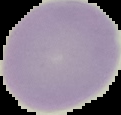
{
  "preparation": "thin blood smear",
  "image_size": "121×115 pixels",
  "malaria_status": "uninfected",
  "image_type": "cell region segmented out of the field of view; surrounding area masked to black"
}